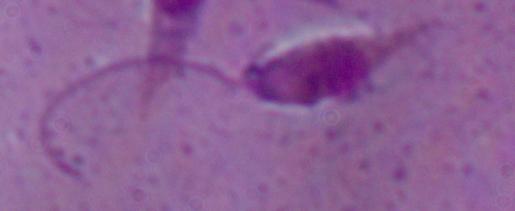

{
  "identification": "Leishmania",
  "modality": "micrograph",
  "magnification": "1000x"
}